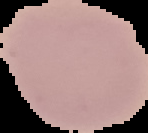

result: no Plasmodium parasites seen
image_type: segmented cell region on a black background
preparation: thin blood film
image_size: 148×133 pixels